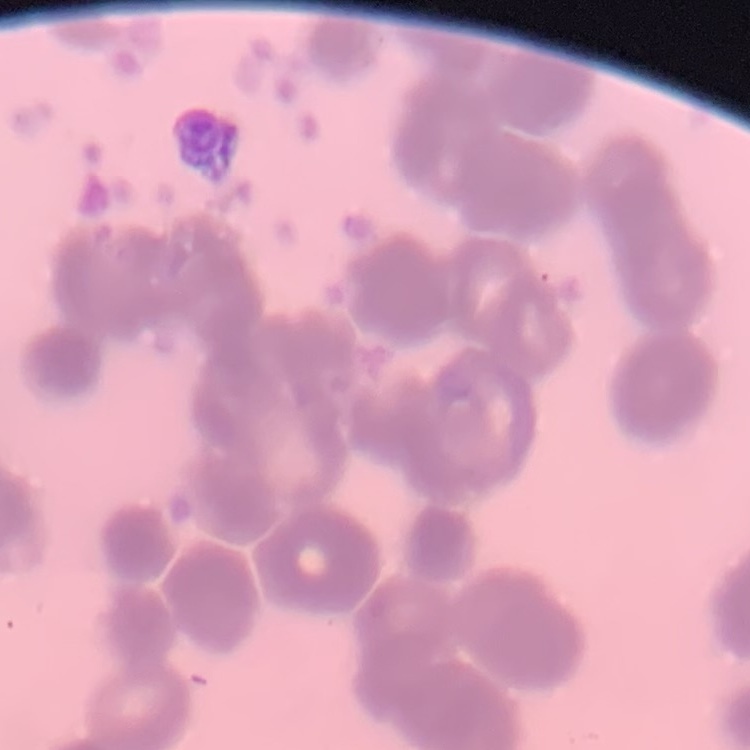

Summary:
  - Red blood cell morphology: rouleaux formation
  - Preparation: thin blood film
  - Stain: Field's or Giemsa
  - Image type: one tile cut from a larger photomicrograph